Classify this cell by malaria status.
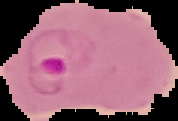
Parasitized.

{
  "image_type": "segmented cell region on a black background",
  "image_size": "178×121 pixels",
  "preparation": "thin blood smear"
}